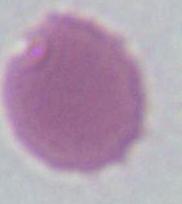

Summary:
  - Magnification: 1000x
  - Identification: erythrocyte
  - Modality: photomicrograph